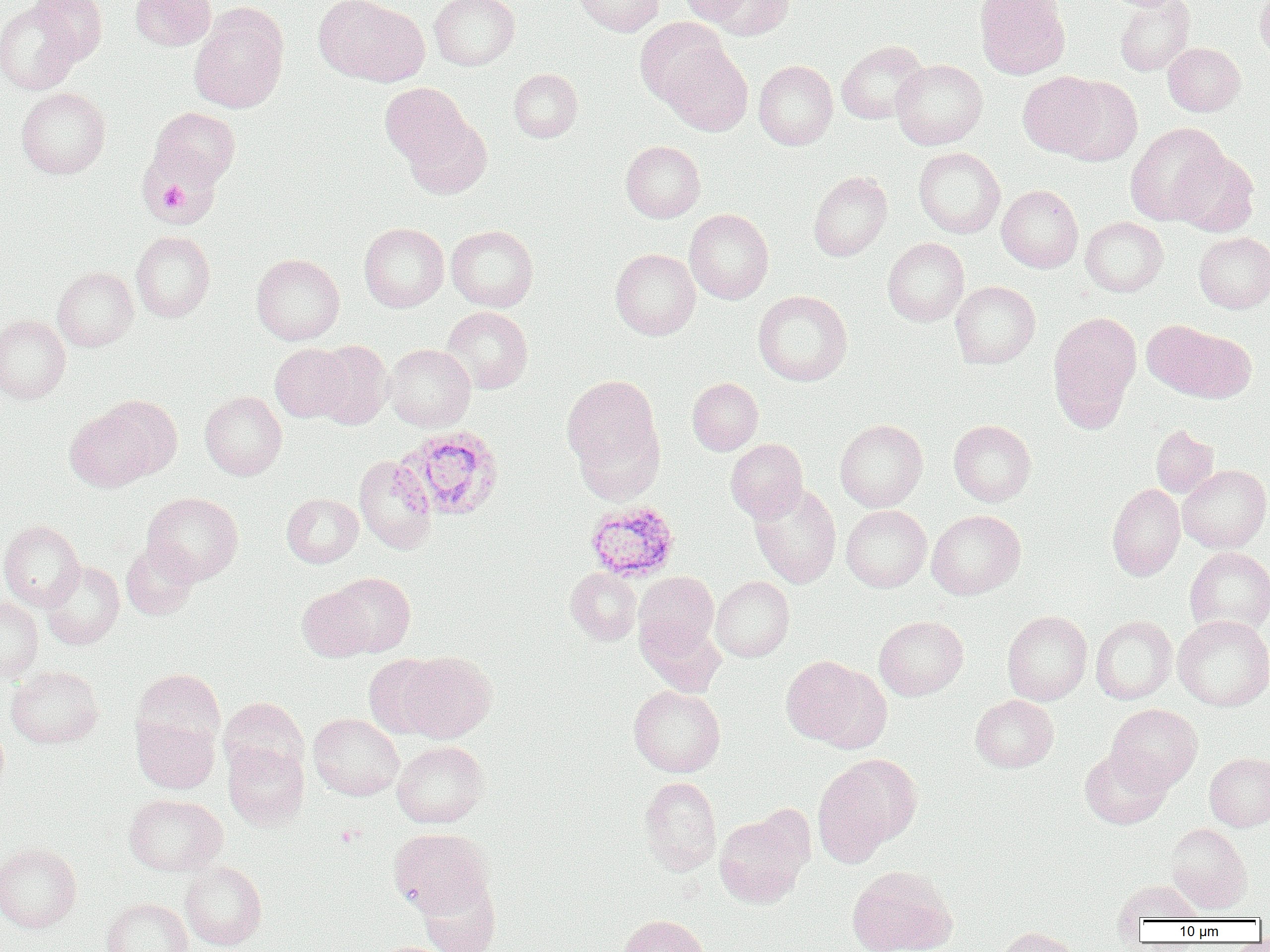
Approximate bounding boxes as named x1/y1/x2/y2 corners in pixels. Platelet locations: (x1=156, y1=182, x2=191, y2=212). Uninfected red blood cell locations: (x1=29, y1=0, x2=107, y2=64), (x1=130, y1=0, x2=216, y2=50), (x1=313, y1=0, x2=429, y2=87), (x1=429, y1=0, x2=520, y2=70), (x1=575, y1=0, x2=664, y2=36), (x1=678, y1=0, x2=754, y2=24), (x1=701, y1=0, x2=793, y2=39), (x1=974, y1=0, x2=1070, y2=79), (x1=1256, y1=0, x2=1270, y2=65), (x1=1114, y1=1, x2=1194, y2=75), (x1=0, y1=2, x2=82, y2=94), (x1=189, y1=3, x2=289, y2=114), (x1=635, y1=18, x2=730, y2=108), (x1=836, y1=40, x2=928, y2=124), (x1=1163, y1=42, x2=1245, y2=116), (x1=661, y1=44, x2=752, y2=136), (x1=891, y1=59, x2=987, y2=149), (x1=753, y1=60, x2=837, y2=150), (x1=508, y1=68, x2=583, y2=142), (x1=1018, y1=72, x2=1107, y2=157), (x1=1055, y1=76, x2=1142, y2=165), (x1=380, y1=83, x2=471, y2=168), (x1=16, y1=87, x2=110, y2=178), (x1=150, y1=107, x2=240, y2=187), (x1=404, y1=114, x2=492, y2=200), (x1=1125, y1=122, x2=1229, y2=227), (x1=138, y1=138, x2=222, y2=227), (x1=620, y1=140, x2=705, y2=222), (x1=914, y1=147, x2=1005, y2=238), (x1=1170, y1=148, x2=1258, y2=236), (x1=809, y1=171, x2=892, y2=261), (x1=997, y1=185, x2=1083, y2=273), (x1=684, y1=209, x2=774, y2=304), (x1=1080, y1=216, x2=1168, y2=296), (x1=359, y1=223, x2=449, y2=312), (x1=447, y1=225, x2=538, y2=312), (x1=131, y1=230, x2=215, y2=322), (x1=1194, y1=232, x2=1270, y2=313), (x1=883, y1=237, x2=969, y2=326), (x1=610, y1=248, x2=700, y2=339), (x1=251, y1=254, x2=345, y2=345), (x1=52, y1=267, x2=138, y2=351), (x1=950, y1=281, x2=1040, y2=368), (x1=753, y1=290, x2=852, y2=386), (x1=441, y1=306, x2=533, y2=394), (x1=1048, y1=312, x2=1141, y2=429), (x1=0, y1=314, x2=71, y2=403), (x1=1142, y1=319, x2=1242, y2=400), (x1=312, y1=340, x2=392, y2=428), (x1=270, y1=343, x2=352, y2=422), (x1=383, y1=344, x2=475, y2=431), (x1=562, y1=373, x2=665, y2=492), (x1=688, y1=378, x2=763, y2=455), (x1=200, y1=391, x2=287, y2=480), (x1=65, y1=404, x2=160, y2=491), (x1=835, y1=419, x2=928, y2=512), (x1=948, y1=420, x2=1036, y2=506), (x1=1151, y1=424, x2=1218, y2=498), (x1=726, y1=439, x2=808, y2=521), (x1=354, y1=456, x2=437, y2=554), (x1=1178, y1=465, x2=1270, y2=553), (x1=749, y1=482, x2=841, y2=588), (x1=1107, y1=483, x2=1185, y2=581), (x1=143, y1=492, x2=243, y2=584), (x1=282, y1=493, x2=362, y2=567), (x1=841, y1=505, x2=931, y2=592), (x1=927, y1=510, x2=1025, y2=599), (x1=0, y1=521, x2=85, y2=611), (x1=121, y1=540, x2=198, y2=619), (x1=1184, y1=547, x2=1270, y2=635), (x1=41, y1=561, x2=124, y2=649), (x1=566, y1=568, x2=641, y2=645), (x1=329, y1=572, x2=415, y2=657), (x1=634, y1=572, x2=719, y2=655), (x1=711, y1=576, x2=794, y2=662), (x1=297, y1=585, x2=375, y2=661), (x1=0, y1=596, x2=43, y2=682), (x1=1002, y1=610, x2=1092, y2=705), (x1=1090, y1=615, x2=1177, y2=703), (x1=1172, y1=615, x2=1270, y2=710), (x1=637, y1=616, x2=726, y2=696), (x1=874, y1=616, x2=968, y2=700), (x1=397, y1=651, x2=496, y2=742), (x1=364, y1=655, x2=447, y2=739), (x1=779, y1=655, x2=883, y2=748), (x1=6, y1=666, x2=103, y2=748), (x1=132, y1=668, x2=225, y2=754), (x1=629, y1=685, x2=725, y2=777), (x1=971, y1=695, x2=1058, y2=772), (x1=219, y1=697, x2=308, y2=779), (x1=1106, y1=703, x2=1202, y2=792), (x1=309, y1=713, x2=404, y2=800), (x1=132, y1=715, x2=219, y2=793), (x1=0, y1=722, x2=9, y2=800), (x1=392, y1=740, x2=489, y2=828), (x1=223, y1=741, x2=309, y2=829), (x1=1080, y1=748, x2=1171, y2=829), (x1=1205, y1=752, x2=1270, y2=831), (x1=812, y1=755, x2=921, y2=864), (x1=639, y1=776, x2=721, y2=874), (x1=123, y1=793, x2=227, y2=876), (x1=714, y1=812, x2=809, y2=907), (x1=1165, y1=823, x2=1251, y2=914), (x1=389, y1=828, x2=493, y2=918), (x1=0, y1=842, x2=81, y2=933), (x1=180, y1=861, x2=266, y2=950), (x1=846, y1=865, x2=956, y2=952), (x1=418, y1=878, x2=500, y2=952), (x1=1114, y1=880, x2=1204, y2=924), (x1=101, y1=897, x2=192, y2=952), (x1=620, y1=914, x2=710, y2=952), (x1=995, y1=926, x2=1079, y2=952). Plasmodium ovale-infected red blood cell locations: (x1=395, y1=425, x2=504, y2=521), (x1=585, y1=500, x2=680, y2=582). Slide-level diagnosis: Plasmodium ovale. Thin blood smear. Optical microscopy. One field of a larger specimen. Image is 1270×952 pixels. 1000x magnification.